Comment on the morphology of the erythrocytes.
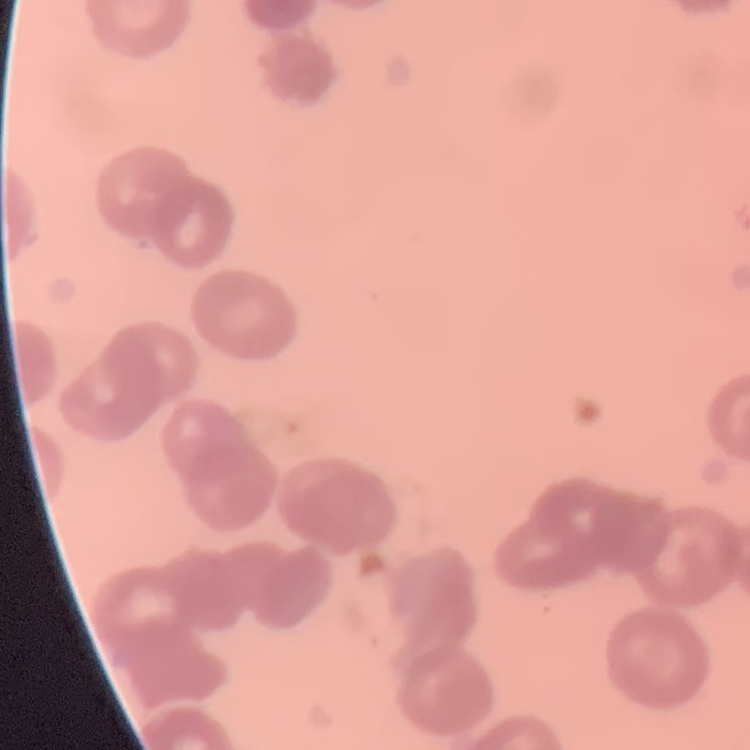
They show rouleaux formation.

image_type: square crop of a larger photomicrograph
preparation: thin peripheral smear
stain: Field's or Giemsa